Outline platelets.
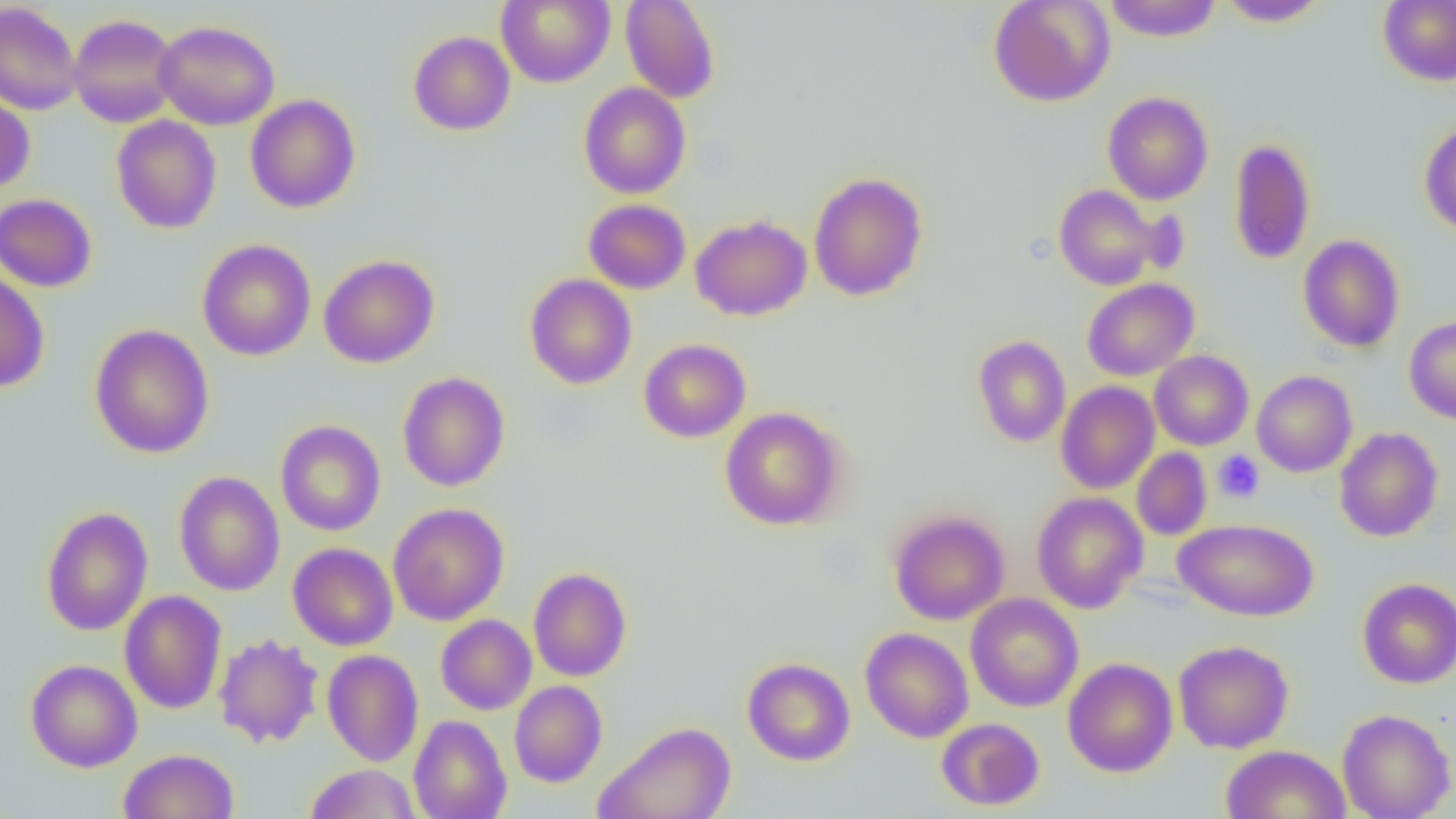
Approximate bounding boxes as (x1,y1)-(x2,y2) corner pairs in pixels.
Platelets: (1213,451)-(1265,503).

Summary:
  - Uninfected red blood cell locations: (496,0)-(615,87), (620,0)-(720,103), (988,0)-(1116,107), (1103,0)-(1223,42), (1217,0)-(1329,27), (1378,0)-(1456,86), (0,2)-(83,116), (68,14)-(180,127), (153,20)-(280,130), (408,31)-(516,135), (578,82)-(691,199), (1102,91)-(1213,205), (0,92)-(35,193), (245,94)-(361,213), (111,115)-(221,234), (1419,122)-(1456,237), (1228,138)-(1316,266), (808,171)-(928,301), (1054,184)-(1163,290), (0,193)-(97,292), (583,199)-(691,294), (690,215)-(812,321), (1298,234)-(1405,352), (197,239)-(316,361), (318,254)-(439,368), (0,271)-(50,393), (524,274)-(637,390), (1082,278)-(1199,381), (1404,315)-(1456,425), (89,324)-(214,459), (973,335)-(1071,447), (639,338)-(751,442), (1149,350)-(1253,450), (1252,370)-(1357,477), (397,371)-(510,492), (1055,381)-(1160,494), (719,406)-(846,530), (275,420)-(386,536), (1334,427)-(1444,542), (1132,448)-(1212,540), (173,471)-(285,596), (1031,492)-(1148,614), (388,503)-(509,626), (41,506)-(153,636), (888,510)-(1010,625), (1174,518)-(1320,621), (288,543)-(398,651), (528,567)-(632,682), (1357,578)-(1456,688), (119,590)-(227,714), (965,594)-(1083,712), (436,614)-(537,715), (860,628)-(974,743), (214,633)-(323,748), (1173,640)-(1294,753), (322,649)-(424,766), (742,657)-(855,765), (1063,657)-(1178,777), (26,659)-(142,772), (509,680)-(608,787), (1337,708)-(1455,819), (408,715)-(512,819), (936,718)-(1045,811), (596,721)-(737,819), (1220,744)-(1351,819), (119,748)-(238,819), (305,763)-(420,818)
  - Slide-level diagnosis: no evidence of blood parasites
  - Modality: optical microscopy
  - Magnification: 1000x
  - Field of view: one of a larger specimen
  - Preparation: thin blood film
  - Image size: 1456×819 pixels